State which parasite is depicted.
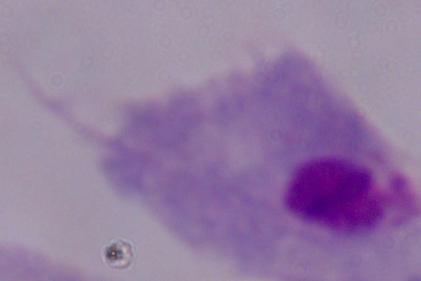
This is a trichomonad.

Summary:
  - Modality: micrograph
  - Magnification: 1000x